State which parasite is depicted.
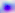

Toxoplasma gondii.

Summary:
  - Magnification: 400x
  - Modality: micrograph